Locate and identify every blood parasite.
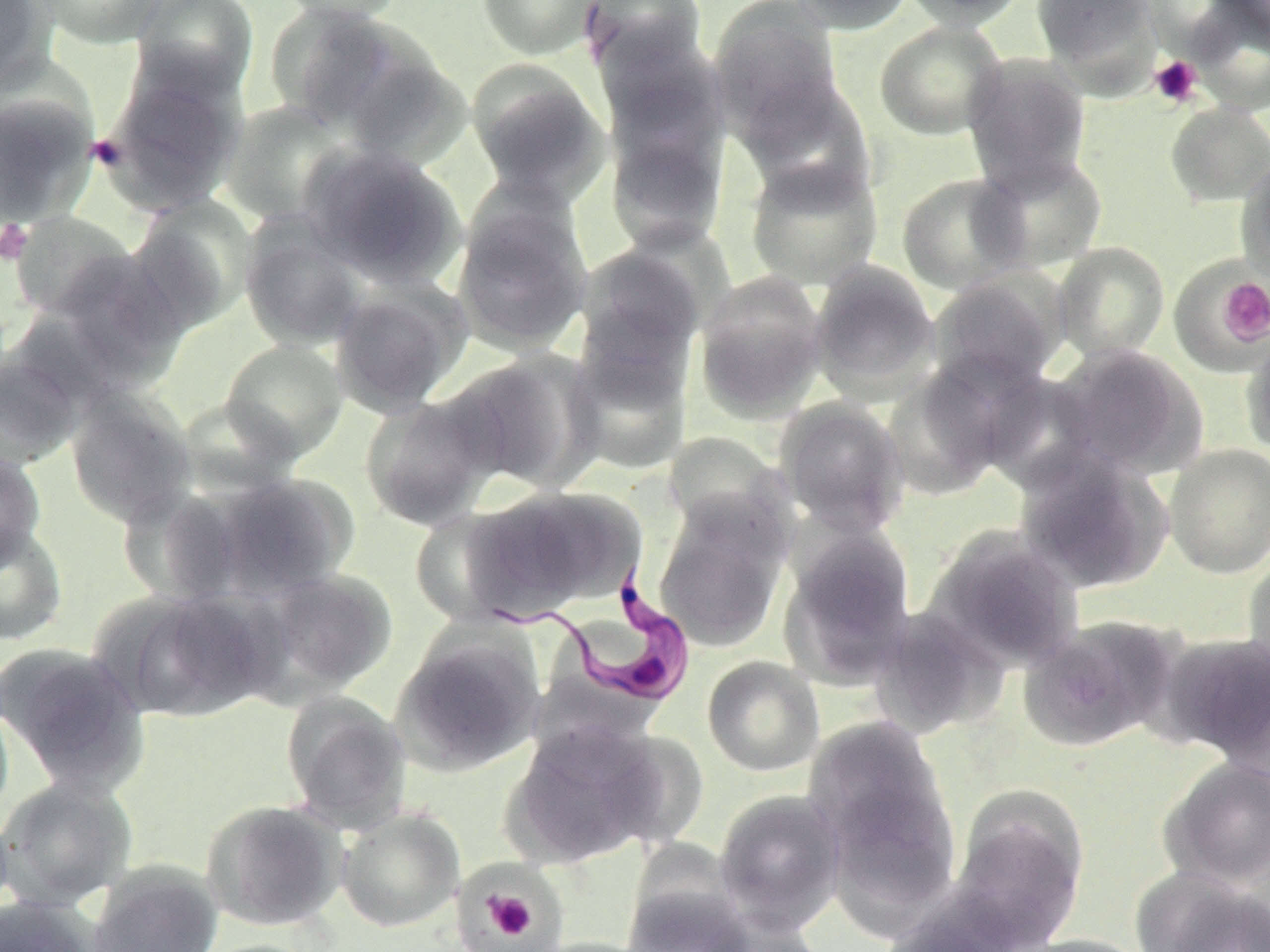

Approximate bounding boxes as (x1,y1)-(x2,y2) corner pairs in pixels.
Trypanosoma brucei: (481,567)-(694,708).
No Plasmodium falciparum, Plasmodium ovale, Plasmodium malariae, Plasmodium vivax, or Babesia divergens observed.

slide_level_diagnosis: Trypanosoma brucei
image_size: 1270×952 pixels
magnification: 1000x
preparation: thin blood film
field_of_view: single
modality: light microscopy
uninfected_red_blood_cell_locations: 'approximate bounding boxes as (x1,y1)-(x2,y2) corner pairs in pixels: (0,0)-(54,91), (29,0)-(167,48), (129,0)-(259,102), (271,0)-(409,23), (476,0)-(603,60), (581,0)-(708,78), (790,0)-(917,34), (898,0)-(1029,30), (1031,0)-(1159,77), (1207,0)-(1270,51), (708,2)-(846,140), (1185,2)-(1270,115), (265,4)-(422,133), (874,20)-(1007,140), (602,55)-(730,237), (961,55)-(1093,195), (99,61)-(247,215), (467,62)-(611,205), (732,70)-(876,201), (0,90)-(98,227), (220,100)-(354,227), (1165,102)-(1270,207), (300,143)-(464,287), (973,151)-(1109,273), (744,156)-(884,290), (1235,157)-(1270,280), (896,172)-(1029,294), (450,190)-(594,356), (127,198)-(258,333), (8,211)-(141,321), (240,217)-(369,351), (575,241)-(711,372), (1053,242)-(1171,361), (41,248)-(190,394), (808,262)-(941,401), (1169,262)-(1268,370), (694,272)-(829,422), (928,272)-(1066,395), (327,277)-(471,416), (1241,335)-(1270,457), (218,339)-(349,462), (566,339)-(694,474), (1049,343)-(1207,479), (452,350)-(604,493), (0,351)-(87,469), (882,365)-(1014,500), (65,389)-(196,527), (359,391)-(505,530), (774,398)-(909,537), (1163,444)-(1270,578), (1013,447)-(1173,594), (0,450)-(46,572), (208,472)-(359,600), (456,484)-(643,620), (116,486)-(247,606), (653,496)-(791,652), (0,521)-(68,646), (921,526)-(1084,674), (779,530)-(917,689), (1241,552)-(1270,682), (248,567)-(398,700), (96,589)-(273,723), (869,607)-(1009,738), (1019,615)-(1183,751), (392,628)-(546,775), (1159,631)-(1270,768), (0,641)-(150,795), (702,655)-(825,776), (280,690)-(412,831), (0,698)-(14,825), (502,717)-(675,867), (803,717)-(961,905), (1157,757)-(1270,890), (0,777)-(138,912), (948,786)-(1090,947), (714,789)-(846,932), (201,799)-(347,932), (335,807)-(466,932), (87,860)-(224,952), (1130,867)-(1269,952), (471,880)-(552,949), (623,883)-(755,952), (0,895)-(102,952), (877,903)-(1021,952), (703,908)-(828,952), (1013,934)-(1156,952), (524,937)-(662,952)'
platelet_locations: 'approximate bounding boxes as (x1,y1)-(x2,y2) corner pairs in pixels: (1149,55)-(1203,108), (88,135)-(126,172), (0,220)-(32,266), (1218,278)-(1270,344), (457,874)-(561,949), (482,890)-(539,942)'
stain: May-Grünwald-Giemsa